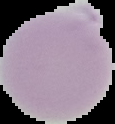
Summary:
  - Image type: segmented cell region on a black background
  - Malaria status: uninfected
  - Image size: 115×124 pixels
  - Preparation: thin blood smear